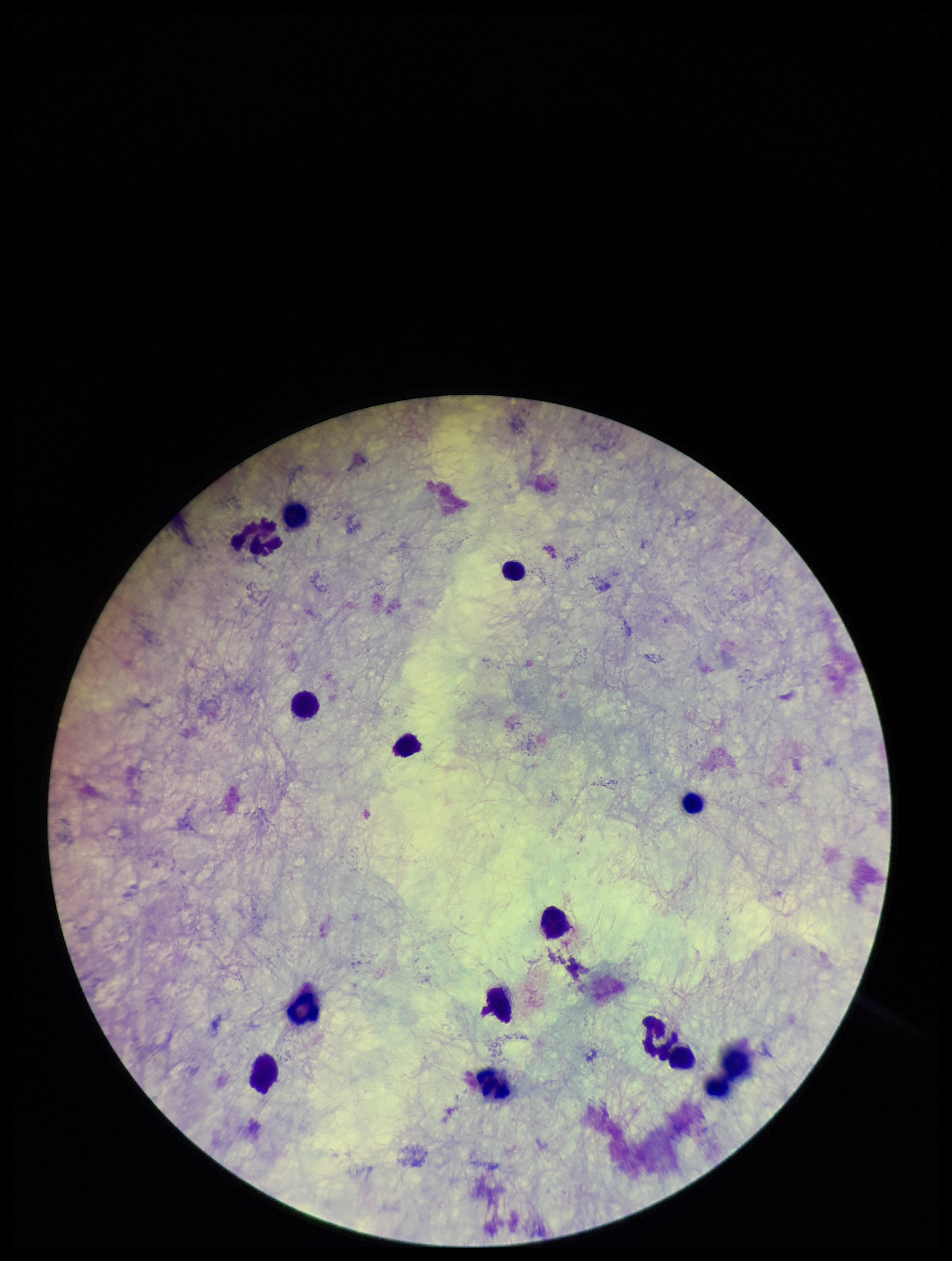

Summary:
  - Capture: smartphone photograph through the microscope eyepiece
  - Patient malaria status: negative
  - Field of view: one from this slide
  - Plasmodium parasites: none detected
  - Leukocyte count: 13
  - Stain: Giemsa
  - Preparation: thick
  - Parasite count: 0
  - Image size: 952×1261 pixels